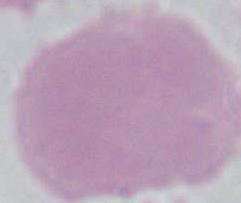

{
  "modality": "photomicrograph",
  "magnification": "1000x",
  "identification": "red blood cell"
}